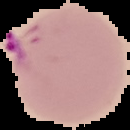
Summary:
  - Result: malaria parasites detected
  - Image size: 130×130 pixels
  - Image type: segmented cell region with the area outside set to black
  - Preparation: thin blood smear